Comment on the morphology of the red blood cells.
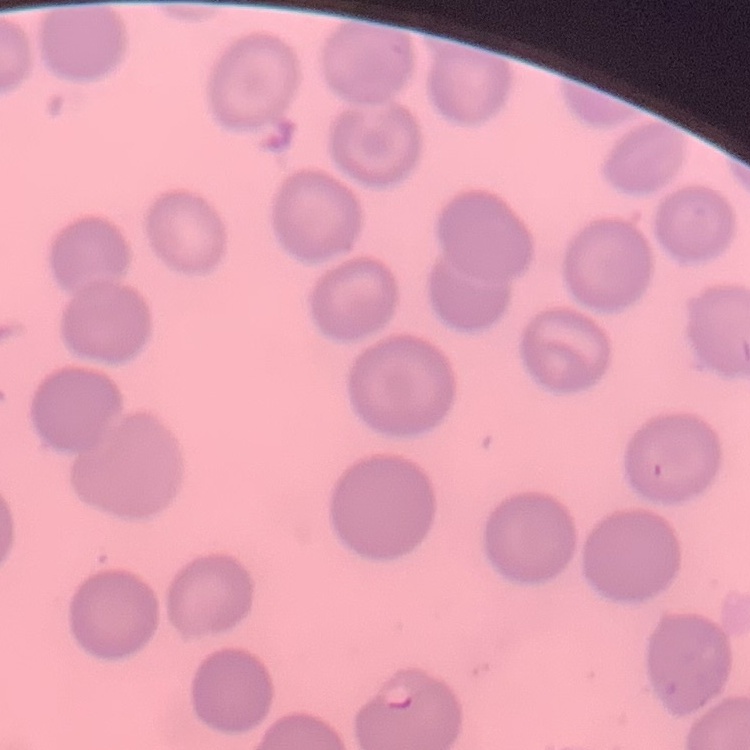

No rouleaux formation.

stain = Field's or Giemsa
image type = square crop of a larger photomicrograph
preparation = thin peripheral smear